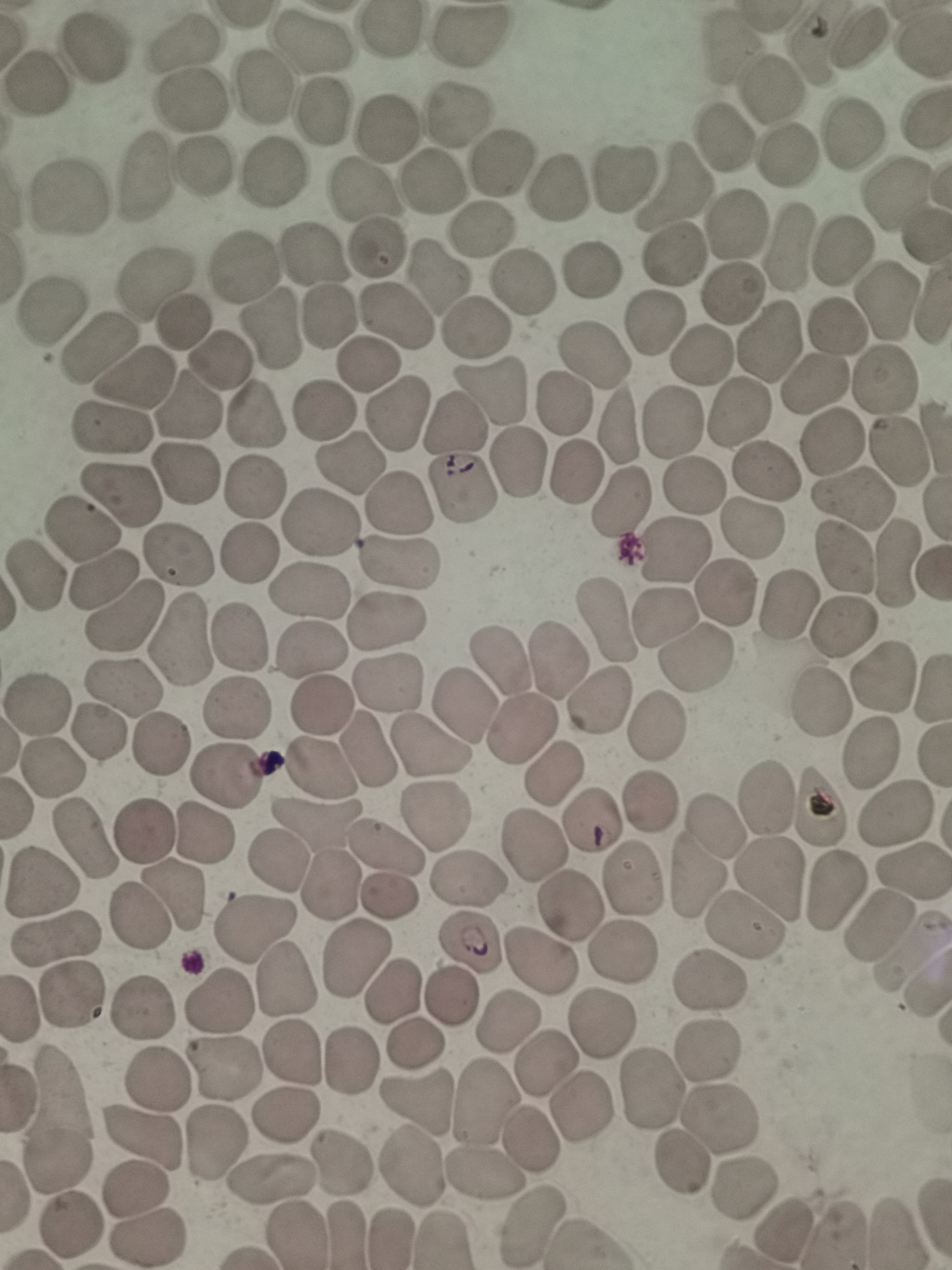

cell_locations: 'approximate object centers, in pixels from the top-left corner: (x=469, y=38), (x=855, y=40), (x=308, y=44), (x=820, y=44), (x=729, y=46), (x=183, y=47), (x=90, y=52), (x=38, y=82), (x=261, y=86), (x=773, y=89), (x=190, y=102), (x=322, y=112), (x=459, y=119), (x=387, y=130), (x=851, y=136), (x=720, y=140), (x=785, y=158), (x=504, y=160), (x=202, y=170), (x=273, y=175), (x=145, y=177), (x=623, y=179), (x=672, y=183), (x=430, y=185), (x=556, y=185), (x=898, y=189), (x=363, y=192), (x=69, y=198), (x=740, y=223), (x=479, y=231), (x=374, y=247), (x=785, y=250), (x=842, y=251), (x=676, y=255), (x=314, y=257), (x=242, y=266), (x=590, y=268), (x=431, y=279), (x=151, y=283), (x=518, y=283), (x=732, y=292), (x=888, y=300), (x=50, y=308), (x=395, y=314), (x=331, y=315), (x=181, y=324), (x=271, y=325), (x=478, y=326), (x=653, y=327), (x=837, y=330), (x=769, y=341), (x=100, y=350), (x=591, y=353), (x=700, y=357), (x=211, y=364), (x=366, y=366), (x=880, y=377), (x=135, y=378), (x=805, y=384), (x=493, y=395), (x=183, y=407), (x=324, y=409), (x=398, y=413), (x=735, y=416), (x=256, y=417), (x=618, y=421), (x=674, y=421), (x=455, y=423), (x=112, y=429), (x=834, y=443), (x=900, y=453), (x=348, y=463), (x=519, y=465), (x=577, y=469), (x=767, y=470), (x=184, y=475), (x=694, y=489), (x=464, y=490), (x=115, y=492), (x=252, y=496), (x=619, y=497), (x=849, y=502), (x=396, y=504), (x=317, y=522), (x=753, y=525), (x=79, y=534), (x=670, y=553), (x=248, y=555), (x=178, y=558), (x=846, y=560), (x=900, y=561), (x=400, y=562), (x=38, y=574), (x=100, y=584), (x=309, y=589), (x=724, y=593), (x=784, y=604), (x=662, y=615), (x=126, y=617), (x=607, y=619), (x=384, y=624), (x=844, y=626), (x=238, y=638), (x=177, y=643), (x=312, y=653), (x=499, y=657), (x=559, y=659), (x=694, y=659), (x=882, y=677), (x=386, y=684), (x=123, y=686), (x=597, y=699), (x=461, y=700), (x=819, y=703), (x=38, y=704), (x=318, y=705), (x=232, y=710), (x=523, y=725), (x=655, y=725), (x=98, y=730), (x=162, y=745), (x=430, y=749), (x=367, y=752), (x=873, y=752), (x=319, y=765), (x=52, y=766), (x=553, y=775), (x=225, y=776), (x=765, y=795), (x=651, y=803), (x=817, y=807), (x=434, y=811), (x=893, y=813), (x=316, y=822), (x=590, y=826), (x=713, y=829), (x=143, y=830), (x=204, y=834), (x=83, y=837), (x=386, y=844), (x=535, y=846), (x=281, y=859), (x=913, y=867), (x=633, y=876), (x=694, y=876), (x=772, y=878), (x=466, y=879), (x=43, y=880), (x=329, y=884), (x=830, y=887), (x=175, y=893), (x=390, y=896), (x=140, y=915), (x=878, y=920), (x=745, y=926), (x=256, y=928), (x=57, y=938), (x=469, y=945), (x=910, y=948), (x=353, y=954), (x=713, y=978), (x=286, y=979), (x=75, y=995), (x=389, y=995), (x=218, y=1001), (x=447, y=1001), (x=140, y=1006), (x=513, y=1022), (x=599, y=1028), (x=414, y=1045), (x=710, y=1046), (x=291, y=1056), (x=348, y=1061), (x=222, y=1067), (x=545, y=1067), (x=157, y=1074), (x=653, y=1093), (x=483, y=1101), (x=413, y=1107), (x=580, y=1108), (x=283, y=1115), (x=61, y=1117), (x=718, y=1121), (x=141, y=1138), (x=215, y=1139), (x=532, y=1143), (x=683, y=1161), (x=345, y=1162), (x=412, y=1171), (x=483, y=1171), (x=273, y=1181), (x=742, y=1185), (x=135, y=1189), (x=531, y=1224), (x=788, y=1226), (x=66, y=1228), (x=148, y=1235)'
stain: Giemsa
preparation: thin smear
field_of_view: single
image_size: 952×1270 pixels
capture: smartphone through the microscope eyepiece